State which parasite is depicted.
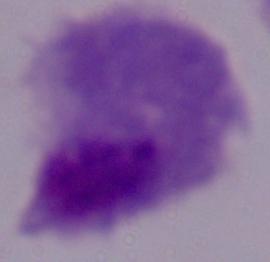

A trichomonad.

Photomicrograph. Captured at 1000x magnification.